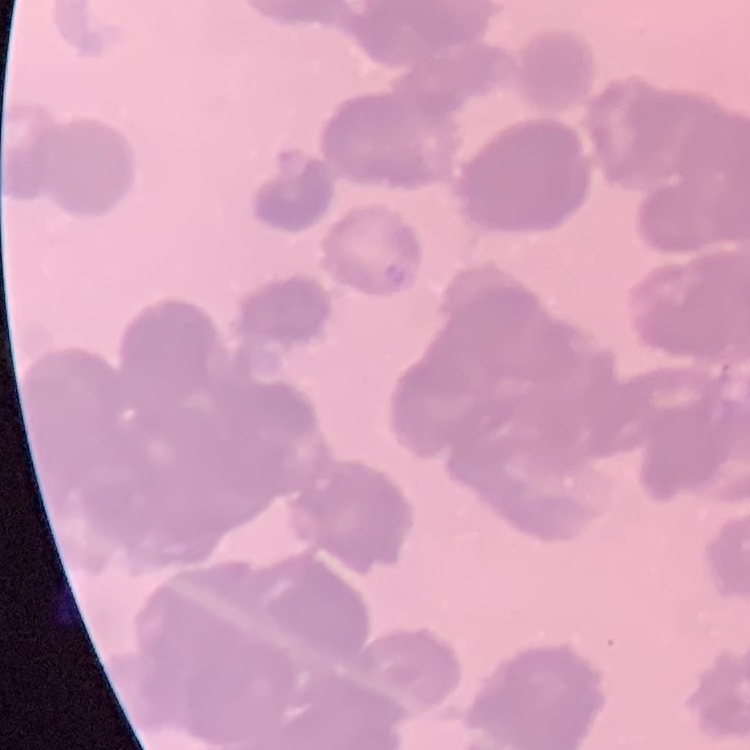
The erythrocytes exhibit rouleaux formation. Thin blood film. Square crop of a larger photomicrograph. Field's or Giemsa stain.